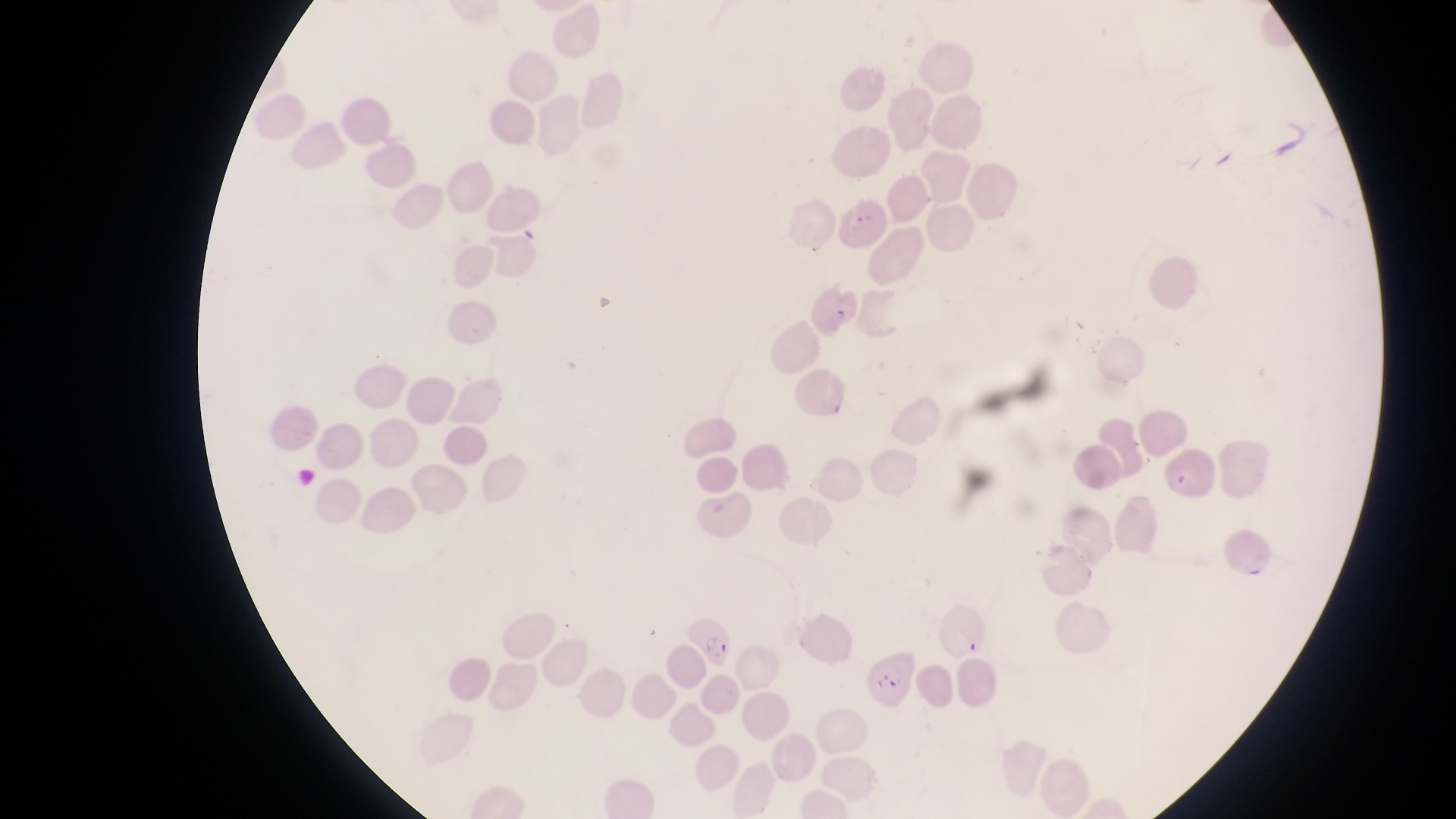

Approximate bounding boxes as [left, top, right, bottom] in pixels.
Summary:
  - Parasitised red blood cell locations: [684, 614, 737, 667], [856, 654, 922, 710]
  - Artifact (platelet-like body, stain precipitate, or debris) locations: [846, 206, 878, 238], [829, 304, 858, 333], [1172, 459, 1198, 492]
  - Preparation: thin blood smear
  - Field of view: single
  - Capture: smartphone photograph through the eyepiece of an Olympus CX-23 microscope
  - Magnification: 1000x
  - Country: Uganda
  - Image size: 1456×819 pixels